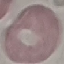
Result: no malaria parasites seen. Acquired by smartphone through the microscope eyepiece. Giemsa stain. Thin blood smear. Automatically extracted cell patch, resized to 64 × 64 pixels.